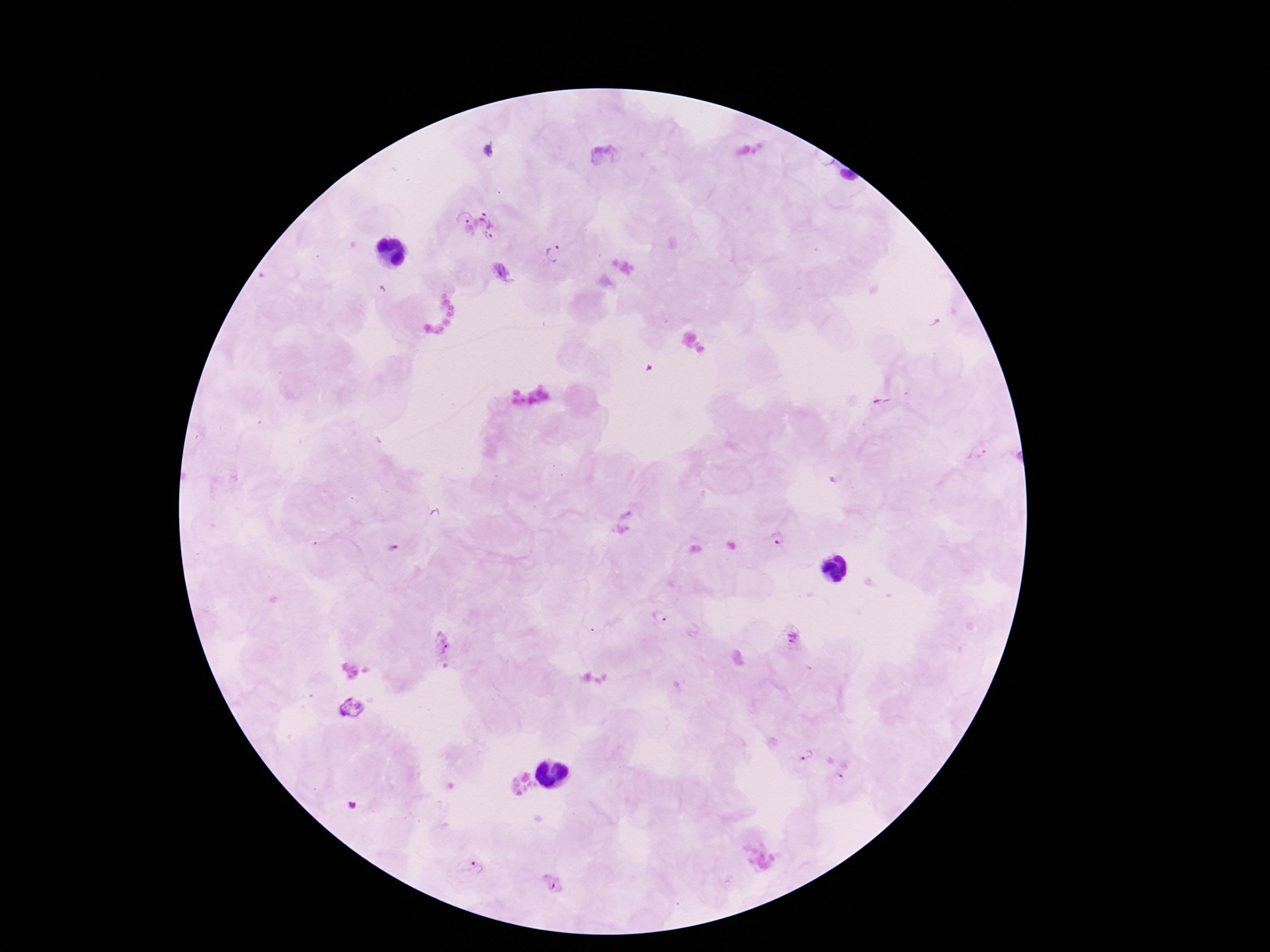
preparation: thick peripheral-blood smear
capture: smartphone camera through the microscope eyepiece
magnification: 100x
stain: Giemsa
field_of_view: single
patient_malaria_status: infected
image_size: 1270×952 pixels
plasmodium_parasite_locations: 'approximate centers as {x, y} in pixels: {489, 150}, {478, 226}, {557, 252}, {881, 401}, {978, 450}, {778, 537}, {660, 619}, {793, 638}, {444, 646}, {806, 752}, {844, 770}, {477, 867}'